Classify this cell by malaria status.
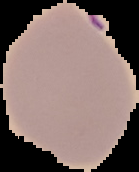

It is uninfected.

Segmented cell region on a black background. Image is 139×172 pixels. From a thin blood film.